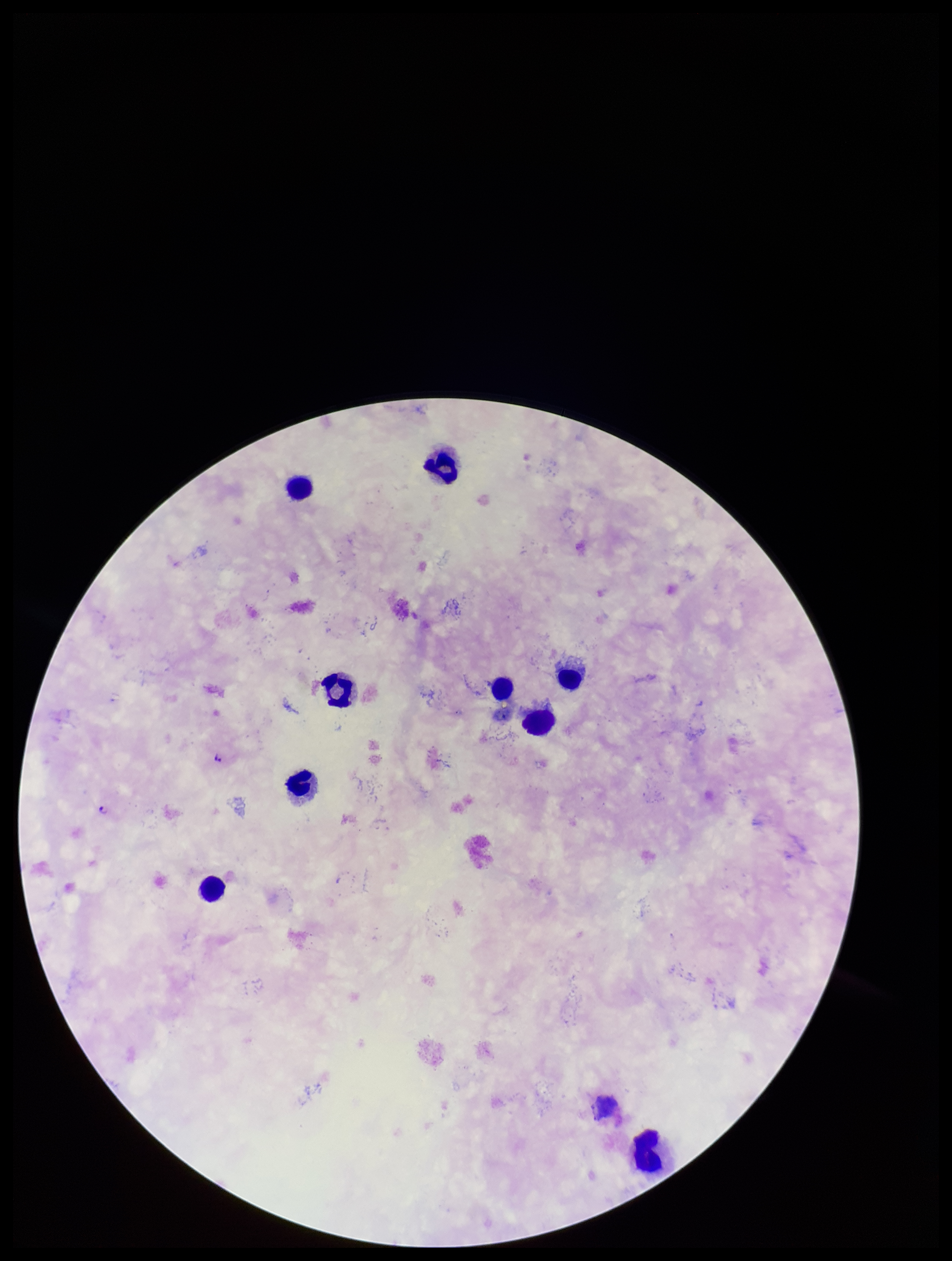
Summary:
  - Plasmodium parasites: detected
  - Preparation: thick
  - Parasite count: 2
  - Stain: Giemsa
  - Image size: 952×1261 pixels
  - Capture: smartphone photograph through the microscope eyepiece
  - Leukocyte count: 9
  - Field of view: one from this slide
  - Patient malaria status: infected
  - Species reported for this patient: Plasmodium falciparum